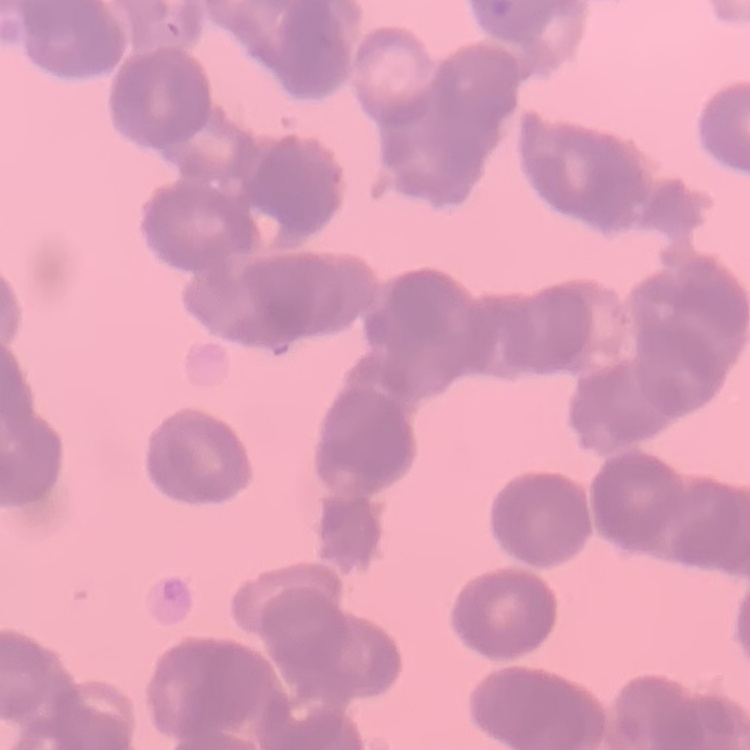

The red blood cells show rouleaux formation. Thin peripheral smear. Stained with either Field's or Giemsa. One tile cut from a larger photomicrograph.